Identify the parasite.
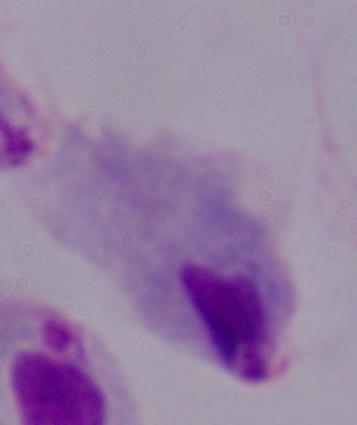
This is a trichomonad.

Photomicrograph. Captured at 1000x magnification.